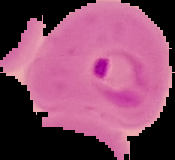

result = Plasmodium parasites detected
preparation = thin blood film
image size = 175×160 pixels
image type = cell region segmented out of the field of view; surrounding area masked to black